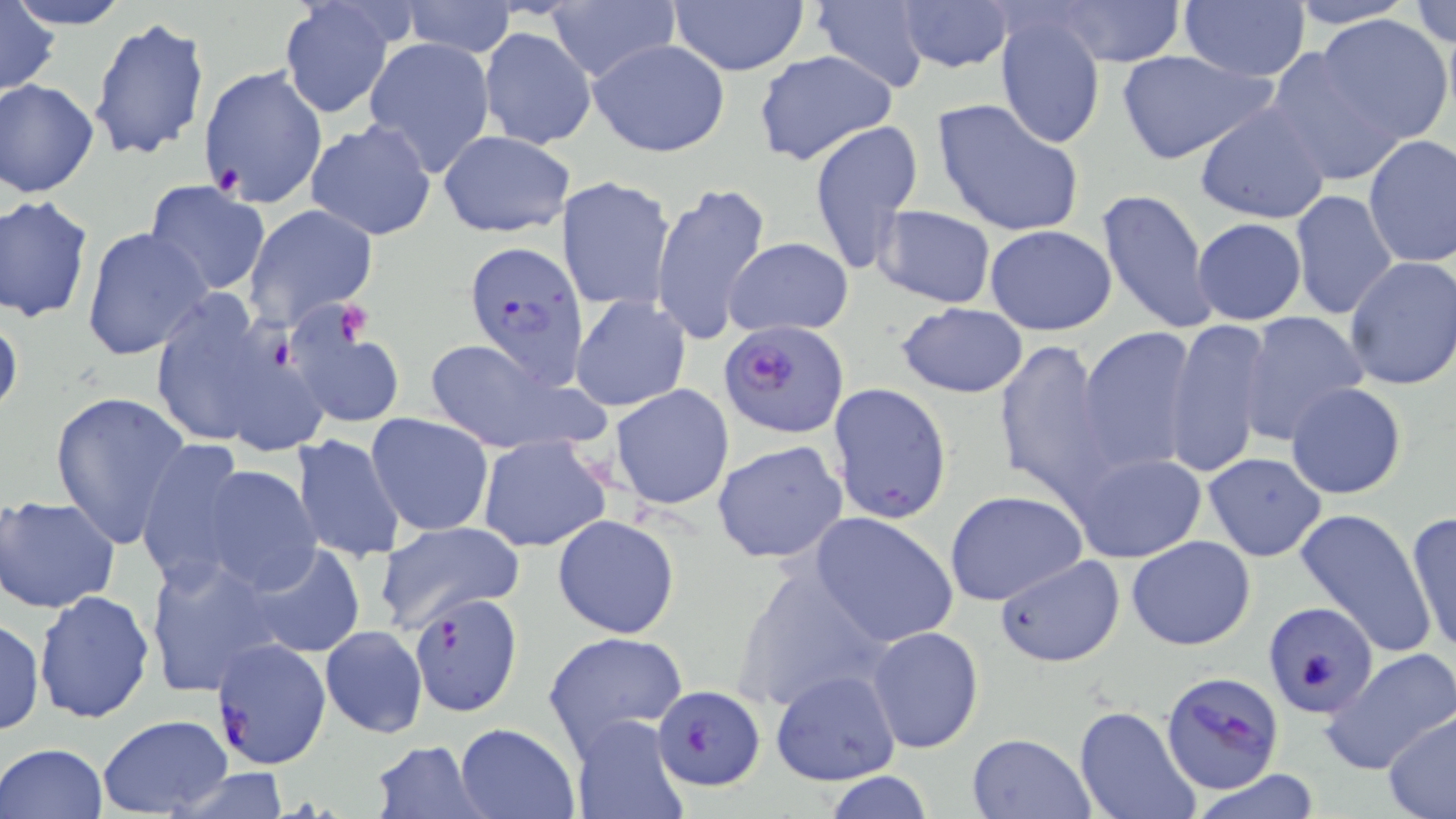

Approximate bounding boxes as [x1, y1, x2, y2] in pixels. Uninfected red blood cell locations: [9, 0, 133, 29], [1054, 0, 1185, 66], [1178, 0, 1313, 82], [1285, 0, 1418, 28], [1411, 0, 1455, 48], [398, 1, 517, 56], [544, 1, 677, 83], [669, 1, 809, 76], [810, 1, 931, 93], [896, 1, 1014, 75], [277, 2, 399, 119], [0, 4, 60, 98], [994, 10, 1107, 150], [1317, 14, 1453, 144], [89, 17, 213, 164], [480, 26, 596, 149], [363, 37, 497, 179], [588, 38, 731, 159], [1264, 48, 1406, 189], [1115, 49, 1276, 165], [752, 50, 900, 168], [198, 64, 328, 207], [1, 78, 100, 199], [931, 98, 1084, 238], [1194, 104, 1330, 224], [305, 119, 437, 241], [807, 119, 924, 274], [438, 129, 575, 238], [1363, 135, 1456, 268], [560, 175, 676, 313], [144, 180, 271, 297], [651, 180, 774, 345], [1097, 187, 1218, 335], [1288, 189, 1398, 323], [0, 195, 95, 323], [244, 203, 378, 331], [871, 205, 998, 309], [1191, 216, 1307, 325], [984, 224, 1117, 336], [82, 226, 212, 362], [723, 238, 854, 337], [1341, 256, 1456, 393], [145, 291, 312, 455], [569, 294, 691, 414], [897, 302, 1028, 398], [0, 310, 23, 420], [1237, 312, 1371, 448], [286, 318, 406, 430], [1164, 319, 1273, 477], [1076, 325, 1200, 475], [421, 336, 602, 455], [993, 337, 1120, 503], [828, 381, 953, 524], [610, 383, 734, 510], [1285, 383, 1406, 500], [49, 391, 192, 551], [366, 413, 495, 537], [292, 432, 407, 565], [476, 435, 612, 552], [135, 439, 251, 593], [712, 440, 848, 565], [1067, 451, 1207, 563], [1201, 451, 1328, 561], [195, 463, 322, 593], [944, 490, 1088, 607], [0, 494, 120, 612], [1293, 506, 1437, 658], [1404, 510, 1455, 657], [809, 512, 959, 648], [552, 513, 681, 638], [376, 520, 523, 632], [1126, 534, 1256, 651], [241, 541, 367, 659], [144, 553, 282, 698], [994, 555, 1124, 668], [731, 563, 890, 716], [34, 589, 156, 723], [1264, 600, 1378, 717], [0, 616, 45, 736], [865, 626, 985, 754], [319, 627, 428, 738], [540, 629, 692, 758], [1321, 647, 1456, 774], [770, 670, 902, 787], [1074, 705, 1201, 819], [1381, 711, 1455, 818], [98, 714, 232, 818], [572, 715, 687, 818], [454, 722, 580, 818], [967, 732, 1095, 819], [369, 738, 490, 818], [0, 742, 110, 819], [1189, 770, 1324, 819], [824, 772, 937, 819]. Platelet locations: [336, 302, 373, 341]. Plasmodium falciparum-infected red blood cell locations: [462, 239, 587, 389], [722, 322, 850, 438], [407, 592, 523, 717], [211, 638, 332, 771], [1159, 669, 1286, 795], [652, 684, 766, 790]. Slide-level diagnosis: Plasmodium falciparum. May-Grünwald-Giemsa stain. Thin blood smear. Image is 1456×819 pixels. One field of a larger specimen. Light microscopy. 1000x magnification.